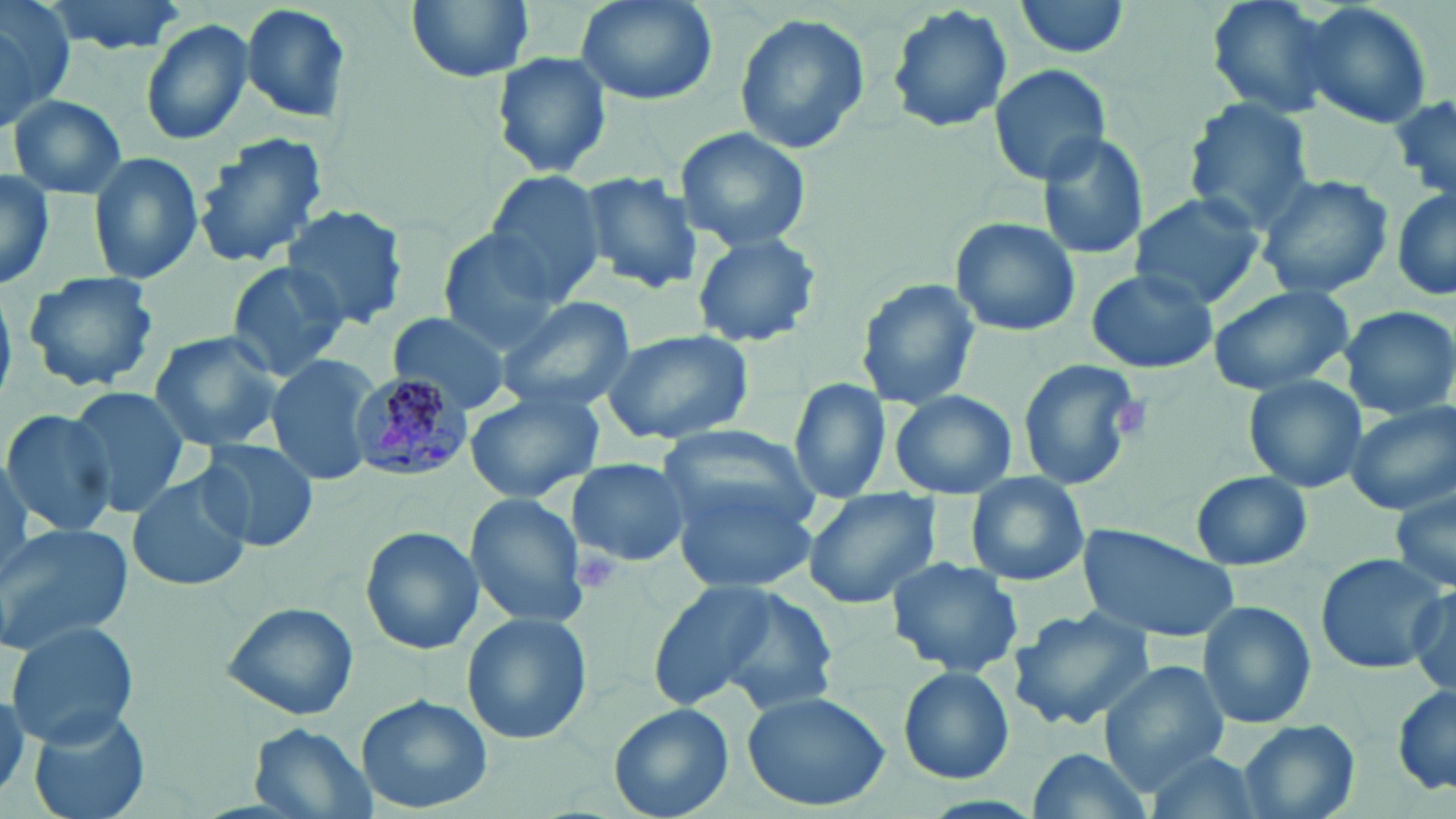

Approximate bounding boxes as [x1, y1, x2, y2] in pixels. Platelet locations: [1114, 392, 1157, 436], [572, 544, 624, 594]. Uninfected red blood cell locations: [41, 0, 191, 55], [406, 0, 536, 82], [574, 0, 719, 107], [1014, 0, 1134, 58], [1206, 0, 1338, 117], [0, 1, 73, 132], [239, 2, 354, 124], [1299, 2, 1434, 132], [885, 4, 1014, 136], [732, 13, 871, 155], [140, 19, 254, 147], [492, 51, 612, 178], [989, 63, 1112, 184], [1388, 91, 1456, 201], [5, 93, 126, 200], [1180, 99, 1316, 232], [673, 126, 812, 251], [1034, 131, 1150, 264], [190, 132, 330, 270], [87, 151, 204, 284], [0, 170, 56, 291], [578, 171, 702, 293], [484, 172, 609, 302], [1256, 173, 1394, 299], [1390, 187, 1456, 305], [1127, 191, 1267, 309], [280, 205, 408, 330], [950, 215, 1081, 337], [435, 228, 571, 349], [691, 231, 821, 348], [221, 258, 350, 384], [1086, 269, 1218, 374], [22, 271, 160, 393], [855, 279, 980, 410], [1206, 284, 1356, 395], [495, 295, 637, 411], [1338, 306, 1456, 420], [385, 310, 515, 414], [601, 329, 757, 446], [148, 331, 287, 453], [264, 353, 380, 486], [1017, 358, 1141, 491], [1243, 374, 1367, 494], [789, 376, 893, 502], [67, 385, 191, 516], [463, 387, 607, 505], [888, 388, 1017, 498], [1345, 403, 1455, 514], [0, 407, 117, 536], [654, 426, 821, 522], [194, 438, 320, 552], [567, 457, 692, 568], [126, 469, 254, 592], [1189, 472, 1314, 570], [962, 475, 1091, 587], [669, 481, 818, 595], [1390, 486, 1456, 595], [801, 488, 944, 610], [463, 493, 590, 629], [1077, 523, 1241, 642], [0, 524, 133, 654], [360, 526, 483, 655], [1313, 552, 1446, 674], [885, 557, 1025, 678], [642, 582, 838, 716], [1406, 585, 1455, 691], [1199, 600, 1317, 728], [220, 601, 359, 721], [1008, 605, 1156, 731], [462, 611, 593, 745], [6, 620, 140, 748], [1098, 660, 1232, 787], [897, 666, 1015, 785], [1391, 686, 1456, 795], [741, 690, 890, 811], [358, 694, 493, 814], [610, 703, 736, 819], [27, 709, 153, 819], [1239, 719, 1360, 819], [247, 724, 377, 819], [1023, 746, 1154, 819], [1141, 750, 1264, 819]. Plasmodium malariae-infected red blood cell locations: [348, 372, 473, 482]. Slide-level diagnosis: Plasmodium malariae. Thin blood smear. Captured at 1000x magnification. Image is 1456×819 pixels. Optical microscopy. One field of a larger specimen. May-Grünwald-Giemsa stain.